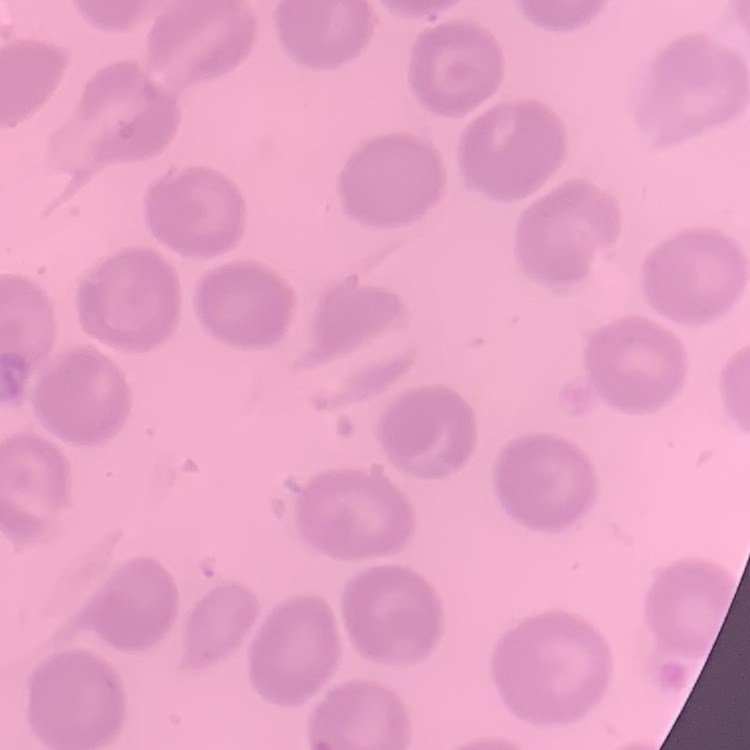

Summary:
  - Erythrocyte morphology: no rouleaux formation
  - Stain: Field's or Giemsa
  - Preparation: thin blood smear
  - Image type: square crop of a larger photomicrograph